Give the extent of all Plasmodium vivax-infected red blood cells.
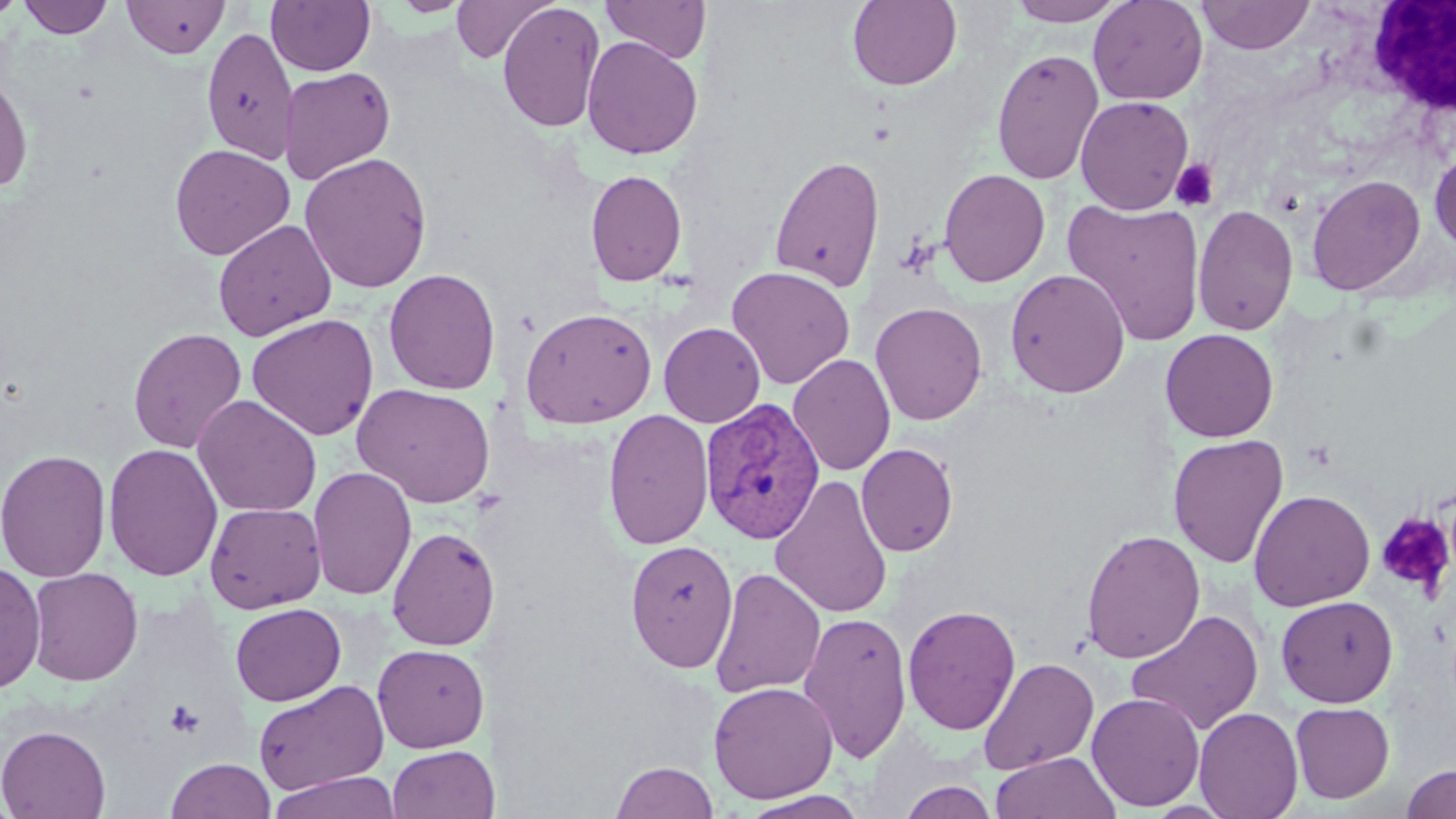
Approximate bounding boxes as (x1, y1, x2, y2) in pixels.
Plasmodium vivax-infected red blood cells: (699, 398, 826, 544).

slide-level diagnosis = Plasmodium vivax
image size = 1456×819 pixels
white blood cell locations = approximate bounding boxes as (x1, y1, x2, y2) in pixels: (1367, 0, 1456, 116)
field of view = single
modality = light microscopy
uninfected red blood cell locations = approximate bounding boxes as (x1, y1, x2, y2) in pixels: (0, 0, 26, 20), (18, 0, 114, 38), (266, 0, 375, 76), (600, 0, 712, 62), (847, 0, 962, 91), (1006, 0, 1129, 26), (1088, 0, 1208, 105), (1196, 0, 1316, 54), (122, 1, 229, 59), (390, 1, 472, 17), (451, 1, 556, 63), (497, 2, 605, 133), (201, 26, 299, 164), (582, 35, 703, 159), (991, 48, 1104, 184), (279, 66, 396, 185), (0, 71, 34, 194), (1075, 95, 1194, 215), (169, 144, 295, 260), (1429, 148, 1456, 252), (298, 151, 433, 293), (770, 154, 885, 293), (585, 168, 688, 288), (938, 168, 1050, 287), (1306, 174, 1426, 296), (1062, 197, 1207, 345), (1192, 203, 1299, 336), (213, 219, 337, 341), (726, 265, 855, 390), (383, 268, 501, 395), (1005, 268, 1130, 398), (870, 301, 987, 426), (520, 306, 658, 429), (245, 313, 379, 441), (659, 322, 765, 428), (128, 327, 247, 453), (1160, 328, 1278, 442), (788, 353, 896, 476), (352, 383, 497, 508), (192, 395, 322, 517), (603, 409, 715, 550), (1168, 433, 1289, 568), (103, 443, 223, 581), (856, 443, 958, 556), (0, 448, 112, 582), (307, 466, 417, 601), (770, 475, 895, 620), (1248, 489, 1375, 611), (205, 501, 327, 613), (386, 525, 501, 651), (1080, 528, 1205, 664), (625, 540, 739, 672), (0, 560, 46, 694), (27, 567, 144, 686), (709, 567, 826, 698), (1275, 595, 1398, 708), (230, 603, 346, 706), (902, 603, 1021, 735), (1125, 609, 1263, 736), (798, 611, 912, 763), (372, 644, 489, 753), (978, 657, 1099, 775), (252, 678, 390, 796), (708, 680, 839, 804), (1086, 691, 1205, 811), (1290, 701, 1395, 803), (1194, 706, 1304, 819), (0, 724, 111, 819), (388, 745, 494, 819), (990, 751, 1121, 819), (165, 757, 276, 818), (610, 760, 720, 819), (1400, 763, 1456, 819), (265, 771, 402, 819), (898, 780, 999, 819), (739, 790, 870, 819)
magnification = 1000x
preparation = thin blood smear
stain = May-Grünwald-Giemsa
platelet locations = approximate bounding boxes as (x1, y1, x2, y2) in pixels: (1170, 159, 1219, 211), (1375, 512, 1455, 597), (163, 699, 206, 738)